Give the position of every Plasmodium parasite.
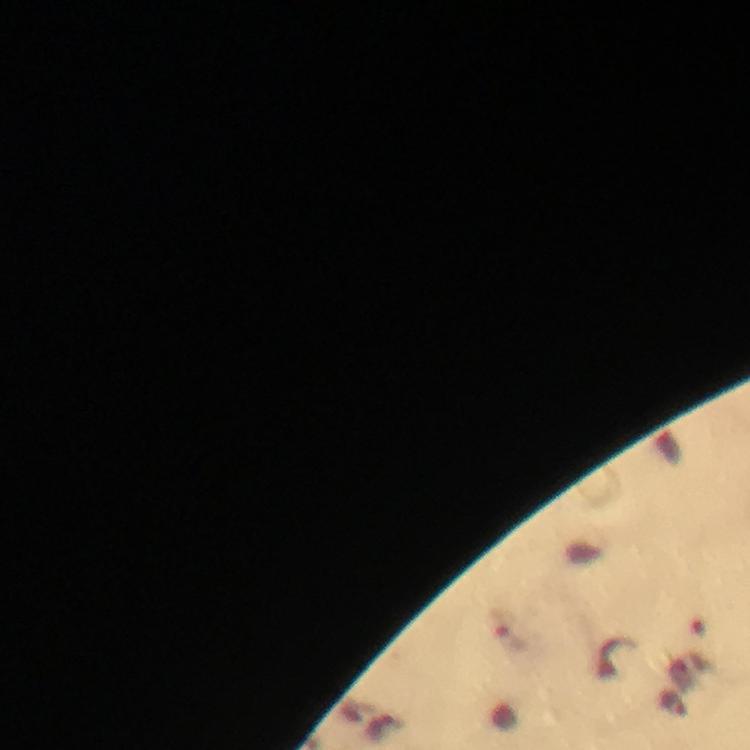
Approximate centers as (x, y) in pixels.
Plasmodium parasites: (506, 632).

{
  "cropped_from": "one field of view",
  "capture": "smartphone mounted on the microscope",
  "magnification": "100x",
  "context": "from a diagnostic examination for malaria",
  "stain": "Giemsa",
  "image_size": "750×750 pixels",
  "preparation": "thick blood film",
  "immersion_oil": "applied"
}